Give the position of every Plasmodium parasite visible.
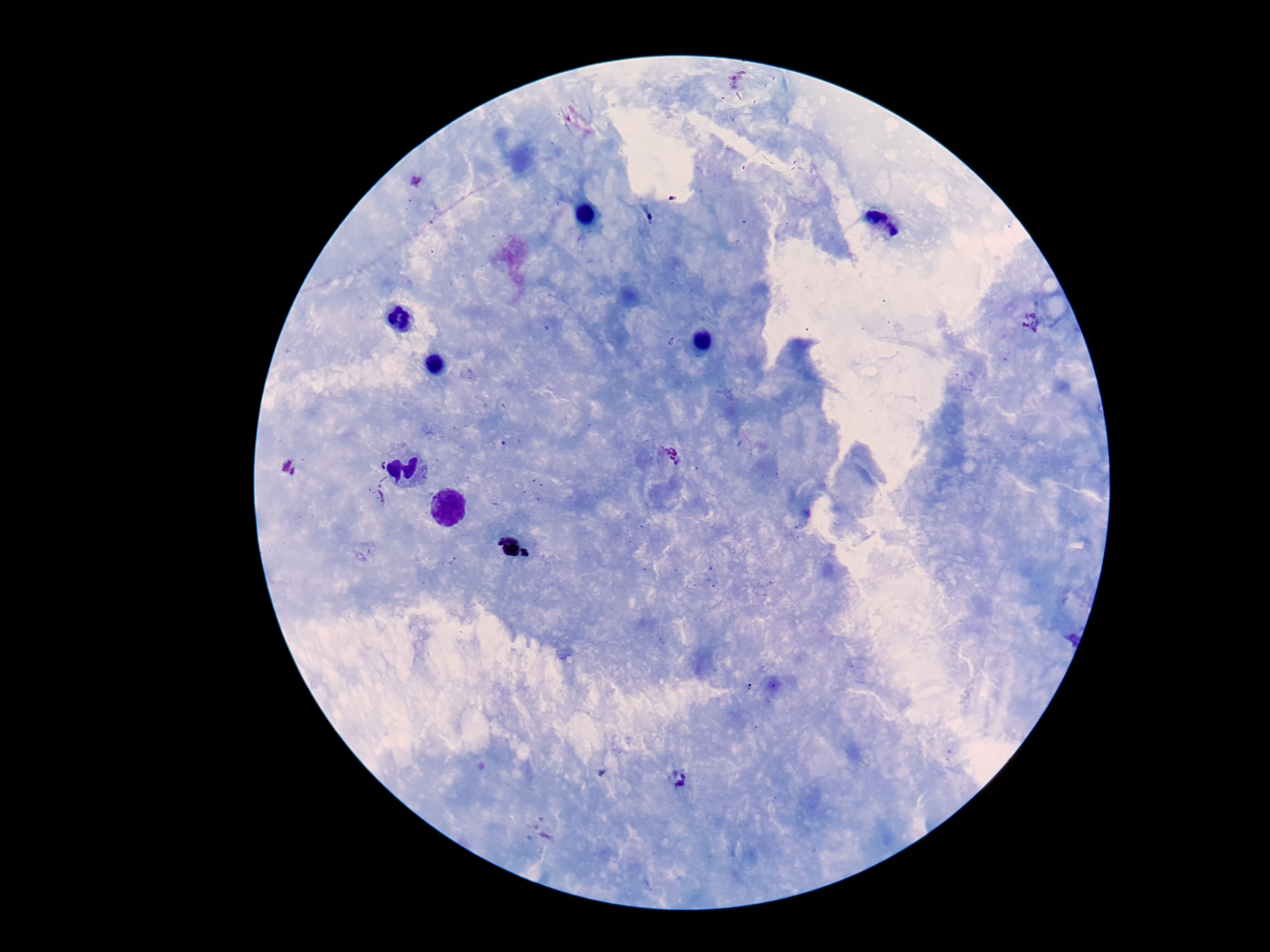
Approximate centers as (x, y) in pixels.
Plasmodium parasites: (1034, 322), (668, 456), (290, 468), (379, 496), (679, 779).

magnification = 100x
stain = Giemsa
capture = smartphone camera through the microscope eyepiece
field of view = single
preparation = thick blood smear
patient malaria status = infected
image size = 1270×952 pixels